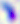

{
  "modality": "micrograph",
  "magnification": "400x",
  "identification": "Toxoplasma gondii"
}